State which parasite is depicted.
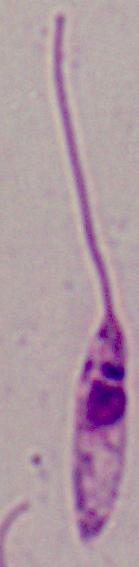
This is Leishmania.

magnification = 1000x
modality = photomicrograph